Report the malaria status of this cell.
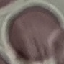
Uninfected.

{
  "capture": "smartphone through the microscope eyepiece",
  "preparation": "thin blood film",
  "image_type": "automatically extracted cell patch, resized to 64 × 64 pixels",
  "stain": "Giemsa"
}